State which parasite is depicted.
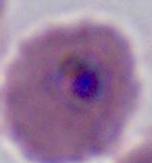
This is Plasmodium.

modality = photomicrograph
magnification = 400x or 1000x